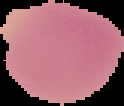

Summary:
  - Malaria status: uninfected
  - Preparation: thin blood film
  - Image type: segmented cell region with the area outside set to black
  - Image size: 124×106 pixels